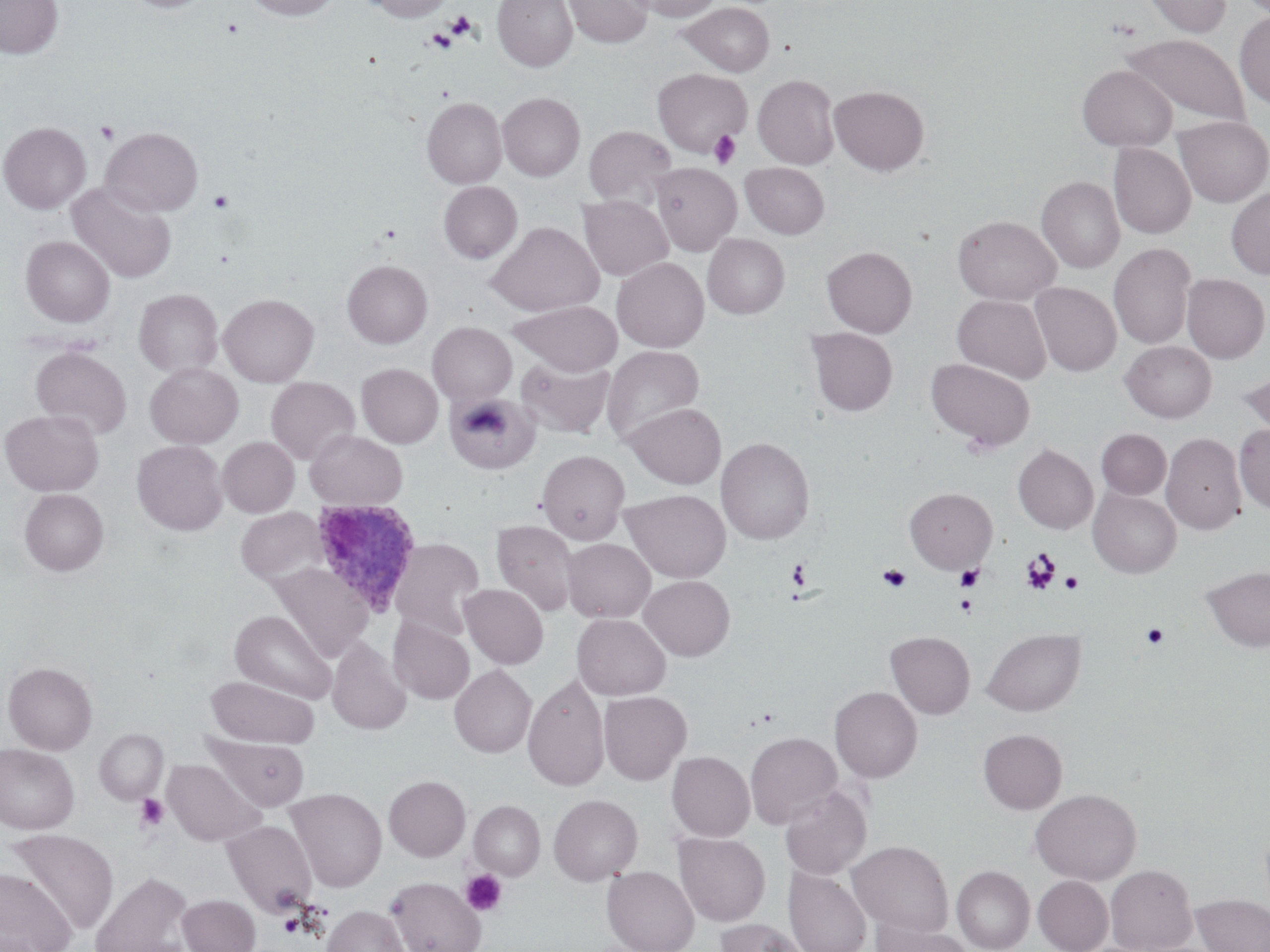
Summary:
  - Coordinate format: approximate bounding boxes as (x1, y1, x2, y2) in pixels
  - Platelet locations: (446, 11, 476, 39), (426, 27, 459, 53), (95, 121, 119, 144), (709, 130, 741, 168), (208, 189, 235, 213), (1020, 548, 1061, 595), (787, 558, 813, 590), (954, 564, 984, 591), (877, 565, 911, 593), (1060, 572, 1083, 595), (956, 595, 977, 616), (1141, 623, 1169, 650), (135, 794, 170, 832), (461, 869, 507, 916), (279, 914, 301, 936)
  - Uninfected red blood cell locations: (0, 0, 64, 59), (122, 0, 214, 14), (245, 0, 340, 20), (362, 0, 455, 22), (492, 0, 577, 71), (563, 0, 652, 48), (629, 0, 722, 21), (1140, 0, 1231, 37), (680, 2, 774, 76), (1234, 11, 1270, 109), (1121, 32, 1251, 129), (1077, 65, 1177, 152), (652, 67, 753, 156), (752, 74, 840, 169), (830, 85, 929, 175), (497, 92, 585, 181), (422, 97, 507, 188), (1173, 116, 1270, 207), (0, 122, 91, 214), (584, 125, 676, 206), (100, 126, 203, 217), (1109, 143, 1195, 239), (741, 162, 829, 239), (650, 163, 741, 255), (1037, 176, 1125, 273), (438, 181, 522, 263), (66, 182, 176, 284), (1226, 187, 1270, 279), (578, 196, 672, 281), (953, 216, 1061, 304), (487, 222, 603, 317), (703, 233, 789, 318), (21, 235, 115, 327), (1109, 244, 1196, 350), (821, 246, 917, 337), (612, 257, 709, 352), (342, 260, 432, 348), (1182, 273, 1269, 363), (1030, 282, 1121, 376), (134, 289, 223, 377), (218, 293, 319, 387), (952, 294, 1052, 384), (510, 300, 622, 376), (427, 322, 517, 405), (806, 327, 898, 416), (1121, 340, 1216, 422), (30, 345, 132, 439), (602, 345, 704, 444), (517, 358, 614, 438), (926, 358, 1035, 452), (145, 363, 243, 448), (357, 363, 443, 448), (1237, 368, 1270, 442), (266, 377, 360, 465), (446, 392, 540, 475), (625, 403, 725, 488), (1, 409, 104, 496), (1234, 424, 1270, 513), (1097, 429, 1171, 499), (305, 430, 407, 511), (1161, 433, 1246, 534), (217, 437, 299, 517), (716, 437, 815, 544), (132, 440, 228, 536), (1013, 444, 1098, 533), (537, 450, 629, 544), (1088, 487, 1181, 578), (905, 488, 997, 573), (19, 489, 108, 575), (621, 489, 731, 583), (236, 507, 328, 586), (491, 519, 579, 617), (388, 538, 485, 638), (563, 538, 655, 622), (270, 563, 373, 662), (1201, 565, 1270, 652), (639, 575, 735, 660), (459, 584, 548, 669), (230, 609, 336, 704), (572, 613, 671, 700), (389, 616, 475, 704), (981, 628, 1086, 716), (983, 629, 1075, 812), (885, 631, 975, 719), (327, 638, 411, 735), (4, 662, 97, 754), (450, 665, 537, 757), (523, 673, 609, 791), (206, 676, 318, 749), (829, 686, 922, 782), (598, 691, 691, 785), (95, 728, 168, 804), (978, 729, 1067, 814), (745, 732, 842, 828), (208, 736, 310, 810), (0, 744, 79, 834), (667, 751, 754, 841), (163, 759, 264, 846), (384, 775, 471, 861), (779, 785, 872, 879), (287, 787, 386, 892), (1030, 788, 1141, 885), (549, 794, 642, 885), (469, 800, 545, 880), (222, 820, 317, 914), (7, 829, 119, 935), (673, 832, 771, 927), (847, 840, 953, 938), (1106, 864, 1197, 952), (952, 865, 1034, 952), (602, 866, 698, 952), (0, 867, 77, 952), (784, 867, 871, 952), (90, 872, 194, 952), (1033, 875, 1113, 952), (386, 877, 487, 952), (177, 894, 260, 952), (1192, 895, 1270, 952), (321, 904, 411, 952), (714, 917, 809, 952), (872, 920, 972, 952)
  - Plasmodium ovale-infected red blood cell locations: (308, 499, 423, 617)
  - Slide-level diagnosis: Plasmodium ovale
  - Stain: May-Grünwald-Giemsa
  - Field of view: single
  - Image size: 1270×952 pixels
  - Modality: light microscopy
  - Magnification: 1000x
  - Preparation: thin blood smear